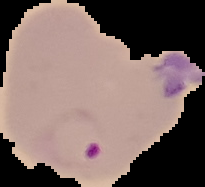

Summary:
  - Image type: cell region segmented out of the field of view; surrounding area masked to black
  - Result: malaria parasites identified
  - Preparation: thin blood film
  - Image size: 205×187 pixels